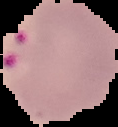
image type = cell region segmented out of the field of view; surrounding area masked to black
image size = 118×127 pixels
malaria status = parasitized
preparation = thin blood film